Comment on the morphology of the erythrocytes.
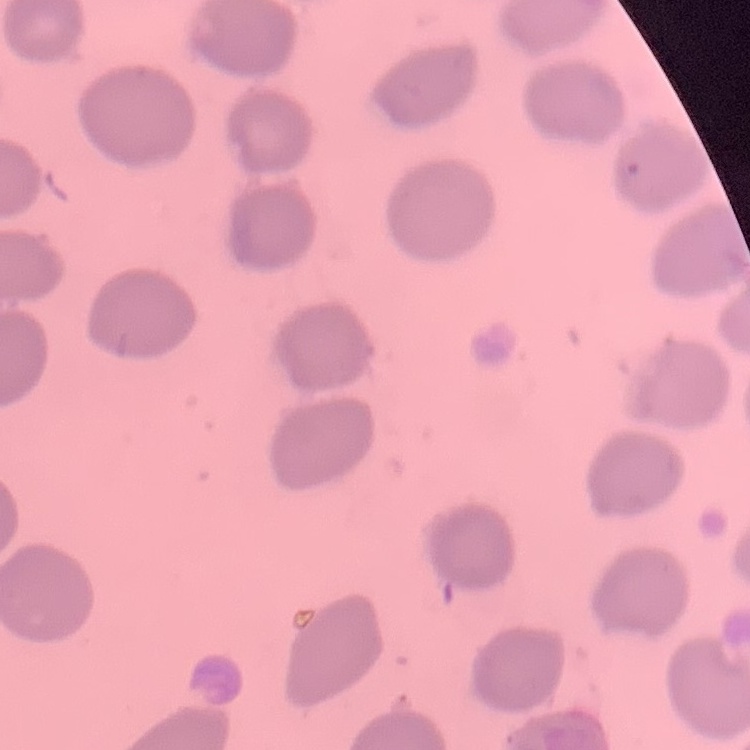

They show no rouleaux formation.

Summary:
  - Stain: Field's or Giemsa
  - Preparation: thin peripheral smear
  - Image type: one tile cut from a larger photomicrograph